Comment on the morphology of the red blood cells.
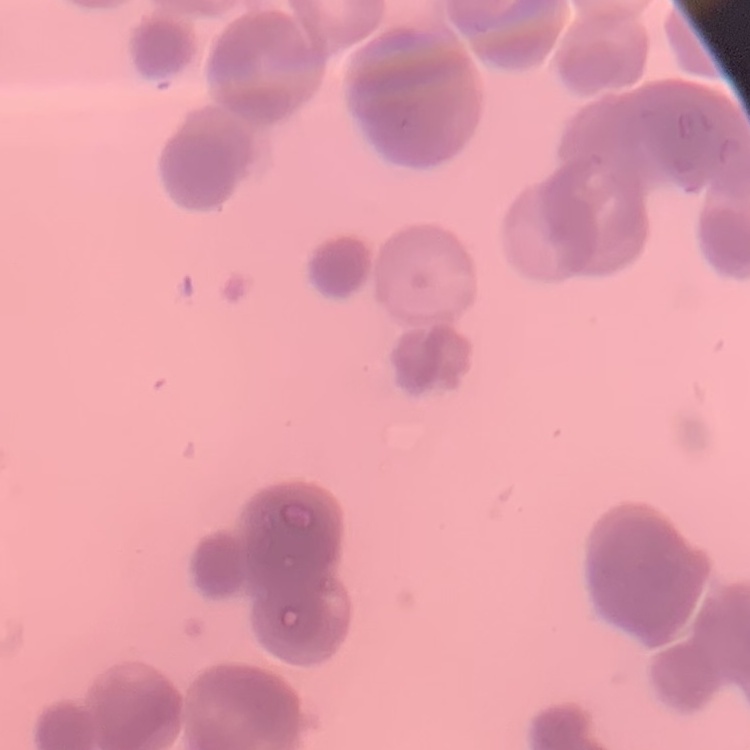
They show rouleaux formation.

Thin peripheral smear. Field's or Giemsa stain. Square crop of a larger photomicrograph.